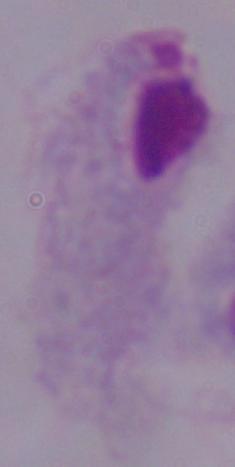

Summary:
  - Magnification: 1000x
  - Identification: trichomonad
  - Modality: photomicrograph